Assess the morphology of the erythrocytes.
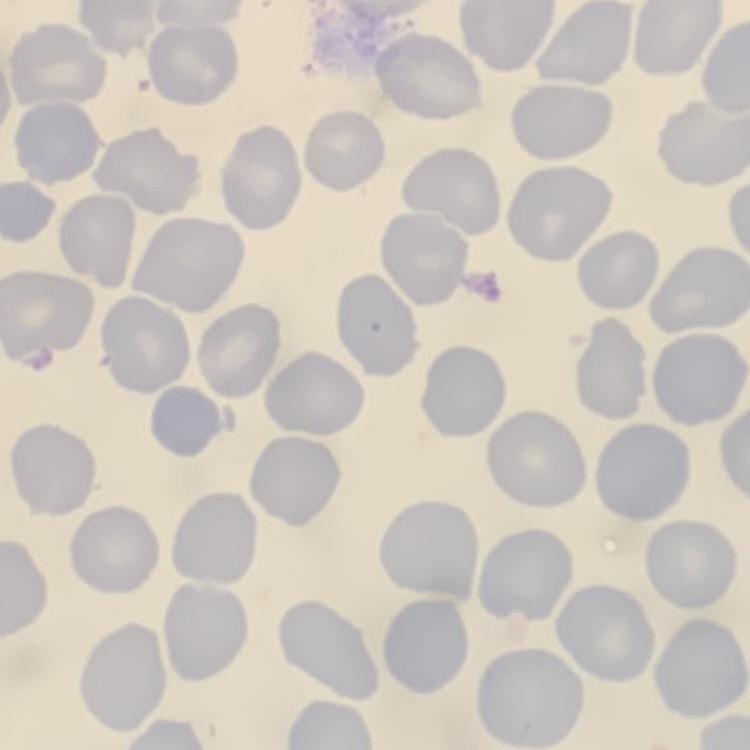

No rouleaux formation.

Field's or Giemsa stain. Thin blood smear. Square crop of a larger photomicrograph.